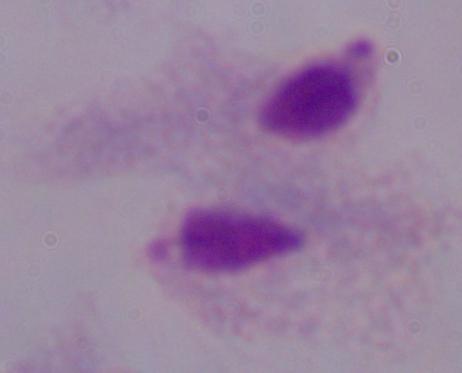
Summary:
  - Identification: trichomonad
  - Modality: micrograph
  - Magnification: 1000x